Report the malaria status of this cell.
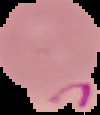

It is parasitized.

Summary:
  - Preparation: thin blood smear
  - Image type: segmented cell region on a black background
  - Image size: 100×115 pixels